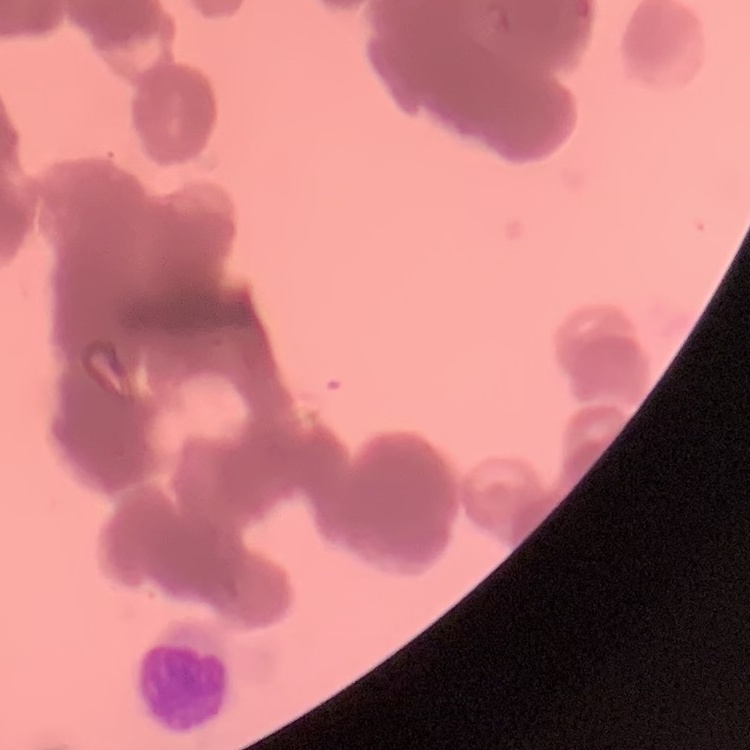

Summary:
  - Erythrocyte morphology: rouleaux formation
  - Preparation: thin peripheral smear
  - Stain: Field's or Giemsa
  - Image type: square crop of a larger photomicrograph